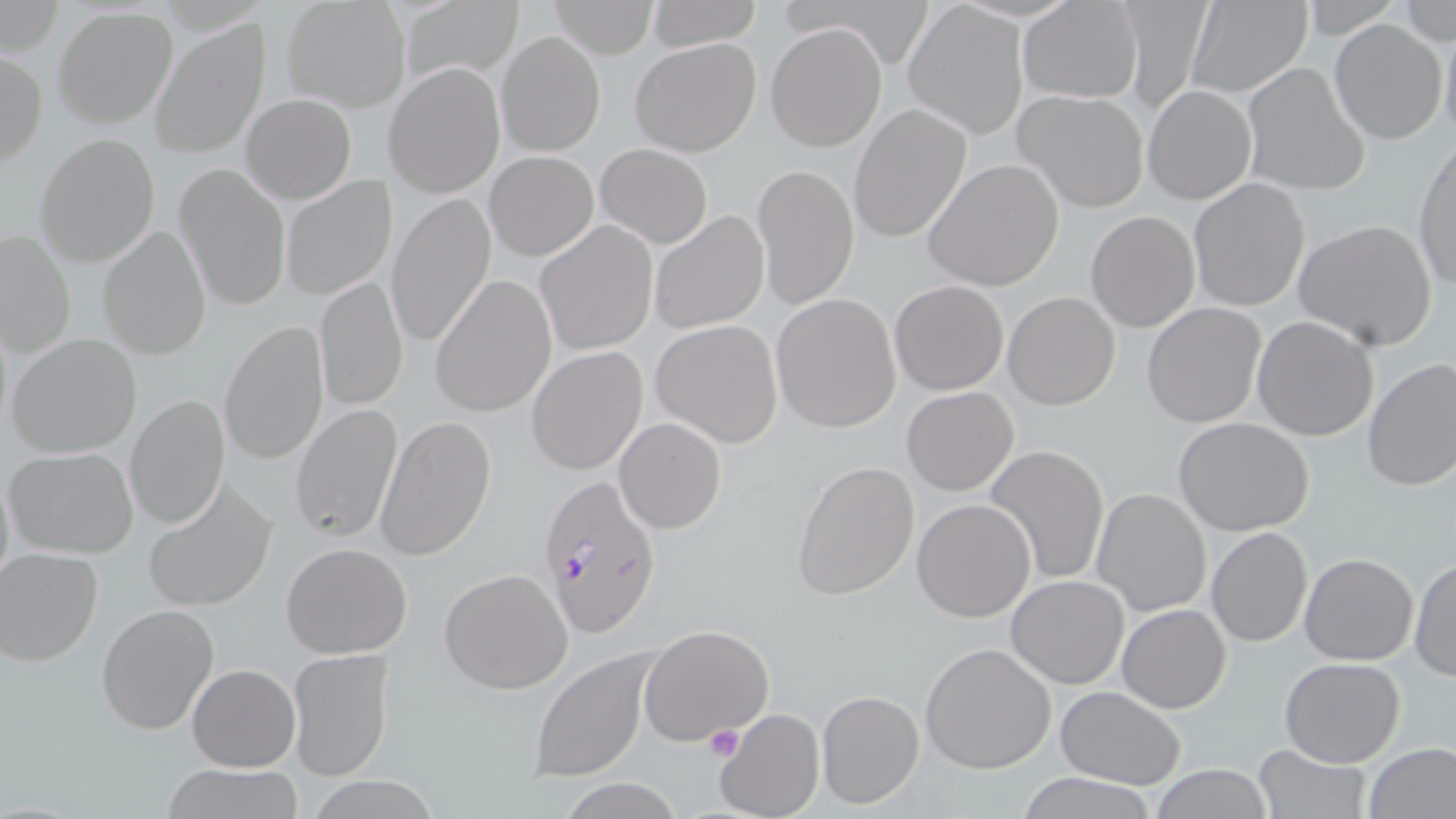

Summary:
  - Coordinate format: approximate bounding boxes as [x1, y1, x2, y2] in pixels
  - Uninfected red blood cell locations: [645, 0, 761, 50], [1117, 0, 1213, 119], [282, 1, 411, 114], [547, 1, 659, 57], [1018, 1, 1143, 102], [1183, 2, 1313, 96], [1402, 2, 1455, 45], [1, 3, 64, 56], [398, 3, 520, 84], [905, 4, 1027, 137], [54, 7, 177, 128], [1329, 18, 1448, 144], [1438, 20, 1456, 148], [151, 21, 268, 158], [766, 22, 888, 152], [495, 31, 605, 157], [630, 36, 761, 157], [0, 52, 47, 167], [383, 62, 505, 198], [1240, 63, 1371, 197], [1142, 84, 1257, 205], [1012, 89, 1150, 213], [241, 93, 355, 203], [848, 103, 972, 244], [35, 133, 160, 267], [1412, 140, 1456, 292], [594, 143, 713, 248], [485, 150, 598, 260], [922, 157, 1066, 293], [753, 162, 859, 310], [174, 164, 291, 312], [278, 174, 397, 301], [1188, 179, 1310, 311], [385, 192, 496, 351], [648, 209, 769, 333], [1086, 210, 1199, 331], [1293, 218, 1438, 351], [536, 220, 658, 356], [98, 224, 211, 360], [2, 230, 76, 357], [431, 273, 558, 417], [314, 276, 408, 412], [889, 279, 1009, 394], [1003, 292, 1120, 409], [771, 293, 901, 433], [1142, 302, 1267, 428], [1251, 315, 1380, 441], [651, 319, 782, 446], [218, 320, 330, 466], [6, 332, 142, 459], [526, 346, 648, 476], [1361, 358, 1456, 493], [901, 387, 1018, 495], [125, 393, 230, 531], [290, 402, 404, 545], [373, 414, 494, 563], [1174, 417, 1318, 536], [615, 418, 726, 533], [982, 445, 1110, 584], [5, 447, 139, 559], [792, 459, 919, 600], [0, 463, 14, 598], [144, 481, 274, 613], [1092, 487, 1212, 617], [912, 499, 1037, 622], [1206, 527, 1313, 648], [281, 543, 412, 658], [0, 547, 103, 667], [1299, 553, 1418, 665], [1409, 556, 1455, 682], [439, 568, 573, 695], [1006, 574, 1130, 689], [96, 603, 220, 735], [1117, 603, 1231, 713], [640, 624, 774, 745], [920, 642, 1058, 773], [286, 648, 395, 781], [528, 649, 654, 782], [1278, 658, 1406, 768], [187, 663, 299, 771], [1054, 686, 1186, 787], [816, 689, 924, 809], [718, 708, 824, 818], [1363, 741, 1456, 819], [1252, 745, 1373, 819], [1150, 763, 1276, 819], [160, 764, 303, 819], [1016, 771, 1156, 819], [310, 775, 438, 818], [559, 778, 685, 818]
  - Platelet locations: [704, 724, 745, 762]
  - Plasmodium falciparum-infected red blood cell locations: [535, 471, 664, 640]
  - Slide-level diagnosis: Plasmodium falciparum
  - Stain: May-Grünwald-Giemsa
  - Magnification: 1000x
  - Modality: optical microscopy
  - Preparation: thin blood film
  - Field of view: one of a larger specimen
  - Image size: 1456×819 pixels